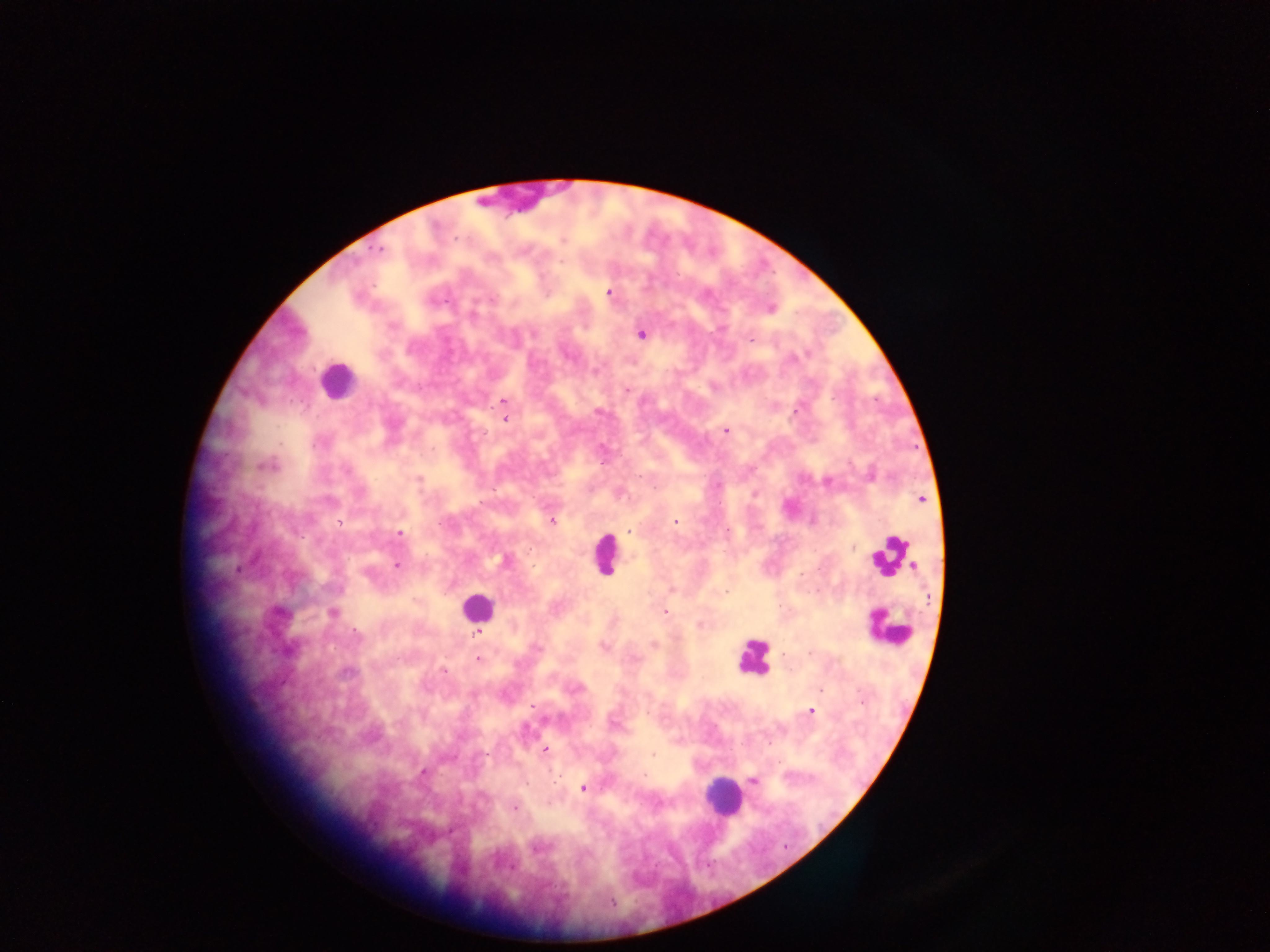 Approximate centers as (x, y) in pixels. Malaria parasite locations: (562, 239), (379, 250), (609, 293), (770, 308), (641, 334), (751, 338), (625, 390), (504, 402), (504, 419), (725, 430), (268, 465), (418, 479), (828, 482), (754, 493), (921, 498), (551, 520), (675, 522), (630, 531), (399, 533), (505, 561), (397, 565), (664, 612), (277, 613), (332, 613), (700, 624), (653, 644), (602, 645), (478, 659), (444, 670), (347, 673), (810, 710), (544, 750), (654, 755), (422, 773), (753, 780), (582, 788), (513, 808). Leukocyte locations: (336, 380), (606, 553), (890, 556), (477, 608), (888, 628), (754, 657), (723, 798). Photographed through a microscope with a mobile-phone camera. Thick blood smear. One field of view. Image is 1270×952 pixels. Sample from Ghana.